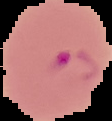 From a thin blood film. Image is 112×121 pixels. Segmented cell region on a black background. Malaria status: parasitized.